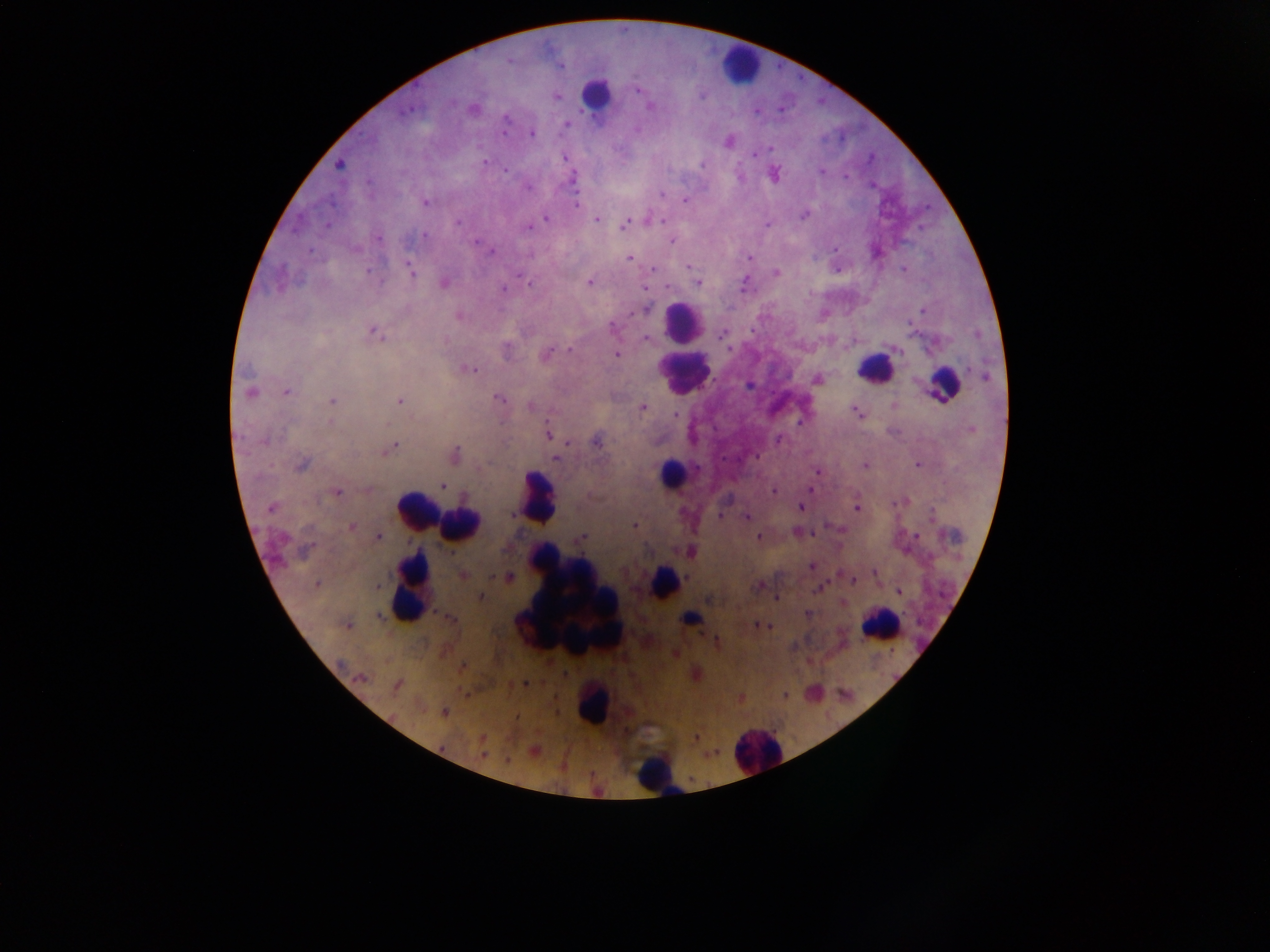 Approximate centers as x y in pixels. Leukocyte locations: 739 65; 595 94; 683 326; 684 368; 874 368; 942 383; 672 472; 539 497; 418 510; 461 525; 664 582; 413 587; 567 602; 689 620; 880 626; 590 705; 757 752; 657 774. Malaria parasite locations: 509 60; 560 66; 637 89; 557 96; 649 107; 408 110; 505 118; 566 125; 503 130; 531 133; 729 142; 771 148; 753 155; 564 157; 485 162; 338 165; 701 165; 505 170; 822 172; 527 188; 662 195; 684 199; 426 203; 576 205; 805 215; 546 219; 597 220; 661 220; 457 222; 625 224; 767 224; 327 226; 528 227; 425 236; 378 239; 476 241; 671 241; 491 251; 749 258; 630 259; 688 267; 903 268; 653 269; 411 270; 369 272; 776 273; 518 275; 445 283; 589 283; 699 283; 745 284; 668 287; 504 290; 645 308; 923 310; 612 327; 373 332; 721 335; 646 339; 570 350; 547 354; 617 355; 471 370; 985 376; 817 379; 287 391; 251 392; 498 398; 332 400; 399 401; 530 406; 643 408; 857 412; 676 414; 329 422; 971 430; 549 434; 778 440; 265 442; 596 442; 566 444; 394 447; 455 454; 555 458; 865 465; 917 465; 302 466; 817 471; 443 486; 810 489; 773 491; 337 492; 801 507; 270 508; 857 508; 511 514; 720 515; 746 517; 635 525; 351 527; 797 532; 917 536; 378 537; 759 537; 581 538; 308 549; 811 566; 875 573; 463 575; 509 577; 853 580; 316 584; 377 587; 819 588; 900 592; 480 597; 777 599; 807 613; 450 618; 349 626; 758 626; 341 663; 463 665; 363 678; 526 683; 396 685; 784 695; 444 713; 481 738; 696 738; 482 755; 506 760. Single field of view. Collected in Ghana. Thick blood smear. Image is 1270×952 pixels. Mobile-phone photograph taken through the microscope.